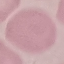 Result: no malaria parasites detected. Thin blood smear. Giemsa stain. Automatically extracted cell patch, resized to 64 × 64 pixels. Acquired by smartphone through the microscope eyepiece.